Assess this cell for malaria.
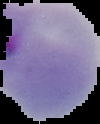
It is parasitized.

Image is 100×124 pixels. Segmented cell region on a black background. From a thin blood film.